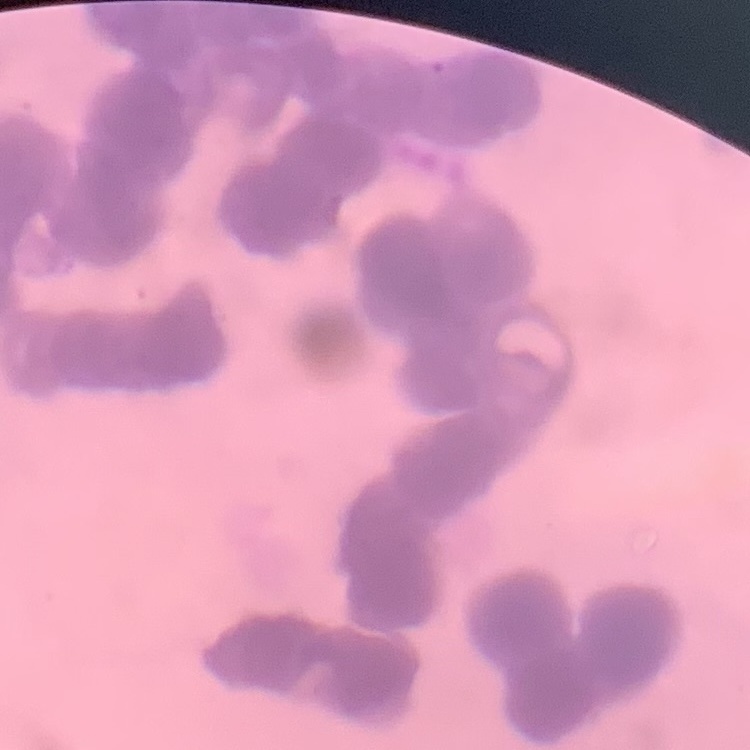
Summary:
  - Erythrocyte morphology: rouleaux formation
  - Preparation: thin blood smear
  - Stain: Field's or Giemsa
  - Image type: square crop of a larger photomicrograph